Outline each Plasmodium falciparum-infected red blood cell.
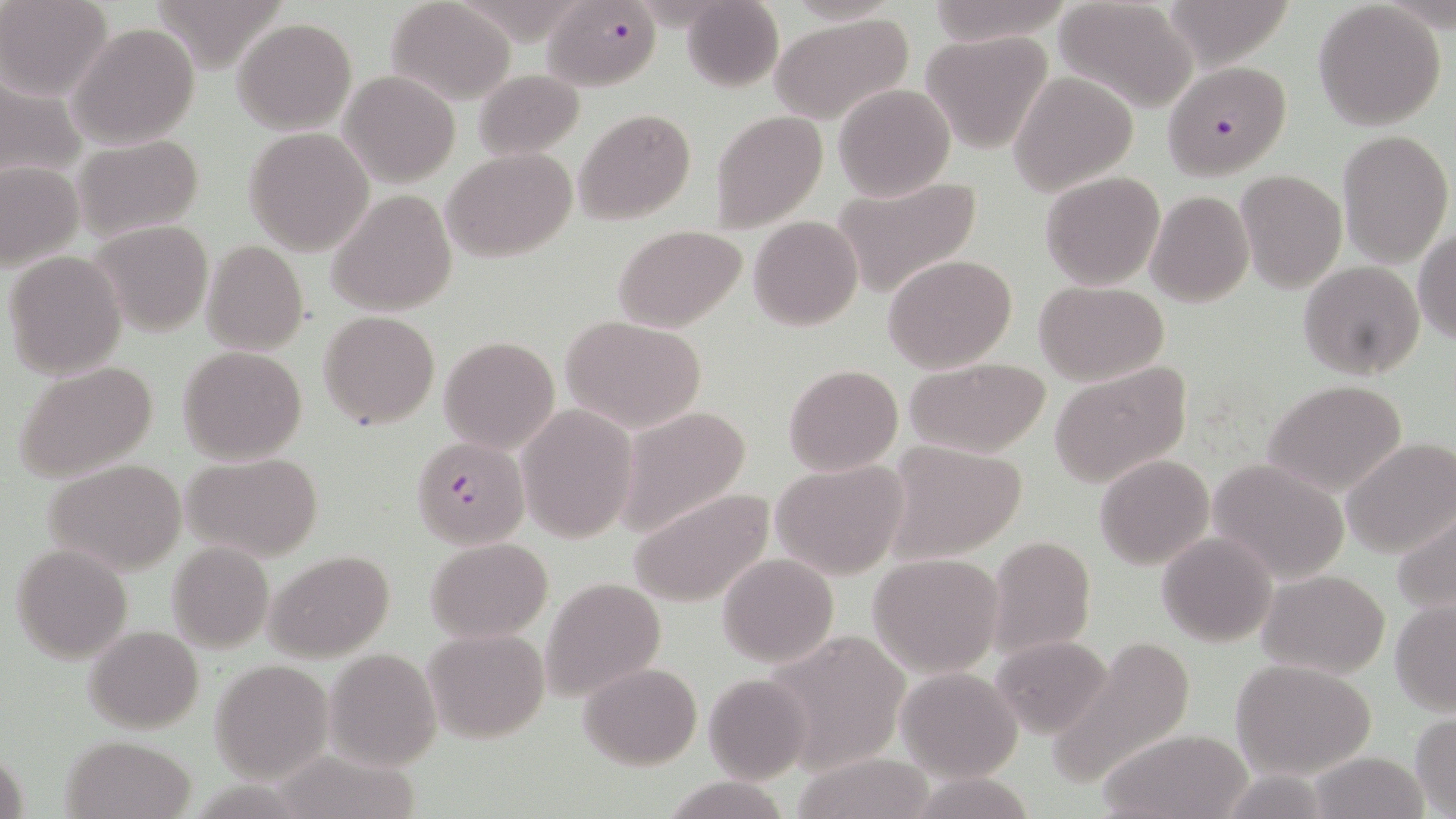
Approximate bounding boxes as (x1,y1)-(x2,y2) corner pairs in pixels.
Plasmodium falciparum-infected red blood cells: (542,0)-(659,90), (1161,61)-(1291,179), (411,437)-(531,556).

Uninfected red blood cell locations: (1,0)-(113,101), (387,0)-(515,104), (681,0)-(783,93), (920,0)-(1072,45), (1054,0)-(1198,112), (1159,0)-(1298,69), (1311,3)-(1448,130), (770,12)-(913,124), (232,18)-(357,136), (67,21)-(201,150), (920,32)-(1054,153), (473,68)-(585,160), (339,71)-(460,189), (1009,72)-(1138,196), (0,77)-(87,183), (834,83)-(956,201), (573,107)-(695,226), (710,109)-(829,233), (244,128)-(373,255), (1336,129)-(1453,264), (71,133)-(204,243), (440,148)-(578,262), (0,161)-(82,270), (1235,170)-(1346,292), (1039,171)-(1166,291), (831,175)-(982,299), (326,190)-(457,316), (1145,190)-(1254,307), (748,216)-(862,332), (88,219)-(214,339), (612,224)-(746,332), (1413,228)-(1456,344), (199,239)-(311,355), (4,250)-(127,379), (883,254)-(1017,374), (1299,262)-(1424,381), (1034,280)-(1170,384), (318,312)-(439,428), (562,316)-(707,432), (439,336)-(560,455), (177,346)-(307,464), (902,356)-(1052,458), (13,360)-(159,483), (1048,362)-(1192,488), (783,363)-(903,476), (1263,381)-(1408,498), (516,403)-(639,543), (615,405)-(753,536), (1343,436)-(1456,559), (878,438)-(1029,565), (180,451)-(324,564), (1094,455)-(1213,569), (43,457)-(190,575), (1208,457)-(1352,586), (769,460)-(908,580), (628,486)-(776,609), (1391,505)-(1456,618), (1157,532)-(1276,647), (986,536)-(1096,659), (426,537)-(551,640), (167,541)-(274,654), (11,543)-(134,664), (266,549)-(395,663), (717,553)-(839,666), (867,553)-(1004,676), (1258,570)-(1390,677), (540,576)-(667,705), (1390,599)-(1456,715), (83,625)-(204,734), (421,628)-(549,745), (768,634)-(913,770), (990,634)-(1114,738), (1044,640)-(1197,788), (324,647)-(442,771), (1229,658)-(1377,782), (209,660)-(333,783), (578,662)-(701,769), (895,667)-(1022,780), (703,674)-(811,782), (1410,712)-(1455,816), (1096,728)-(1252,818), (63,734)-(195,818), (1306,750)-(1428,819), (789,754)-(936,817), (907,773)-(1038,818), (658,776)-(796,819). Slide-level diagnosis: Plasmodium falciparum. Image is 1456×819 pixels. Thin blood film. May-Grünwald-Giemsa stain. Captured at 1000x magnification. Single field of view. Light microscopy.